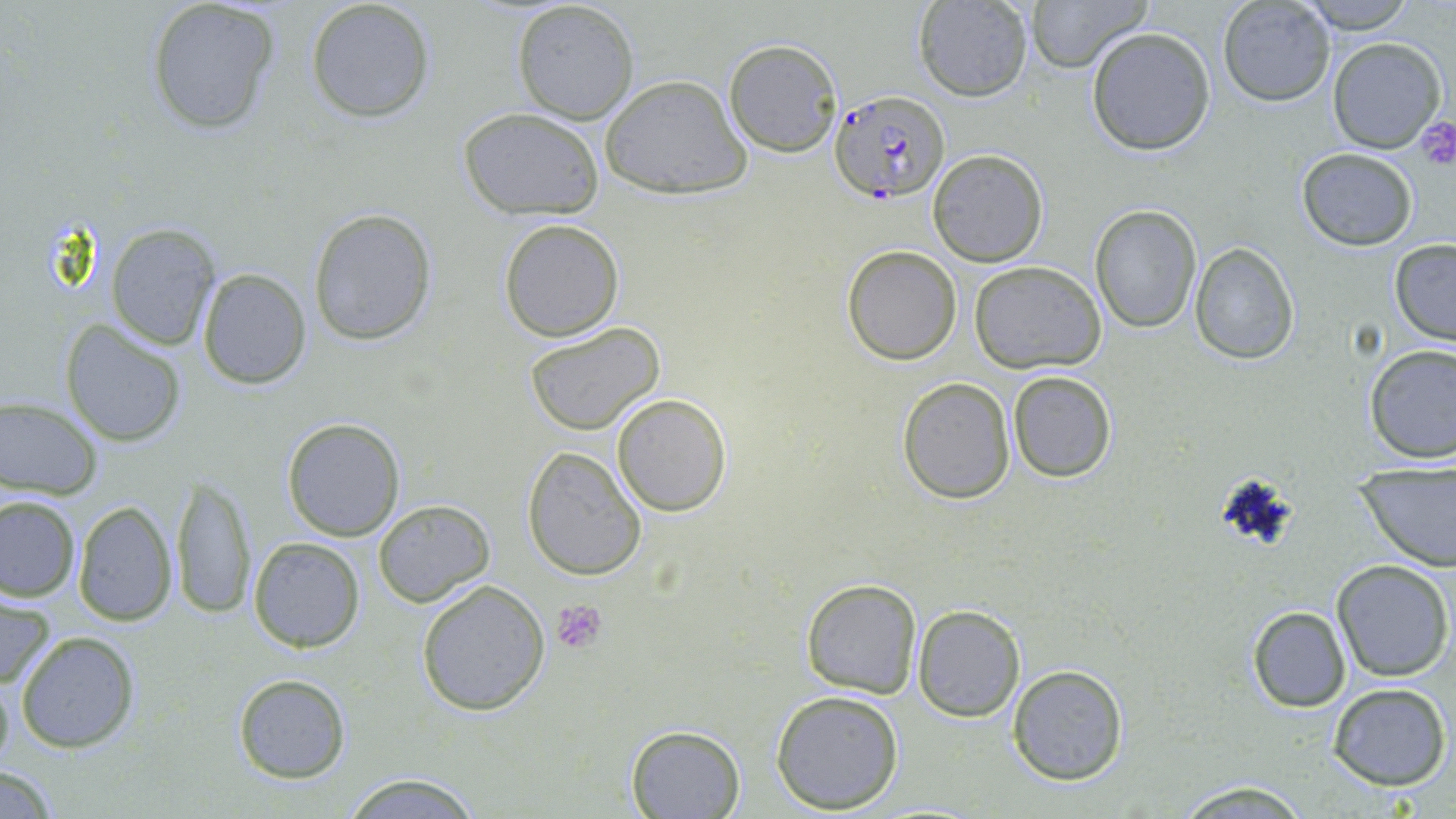

Summary:
  - Coordinate format: approximate bounding boxes as named x1/y1/x2/y2 corners in pixels
  - Uninfected red blood cell locations: (x1=146, y1=0, x2=279, y2=136), (x1=305, y1=0, x2=436, y2=123), (x1=1022, y1=0, x2=1154, y2=73), (x1=1216, y1=0, x2=1336, y2=107), (x1=1297, y1=0, x2=1418, y2=34), (x1=912, y1=1, x2=1034, y2=102), (x1=510, y1=2, x2=640, y2=125), (x1=1086, y1=27, x2=1217, y2=155), (x1=723, y1=37, x2=844, y2=158), (x1=1326, y1=37, x2=1447, y2=154), (x1=600, y1=75, x2=751, y2=199), (x1=458, y1=107, x2=606, y2=218), (x1=1294, y1=146, x2=1419, y2=252), (x1=927, y1=148, x2=1049, y2=267), (x1=1090, y1=204, x2=1202, y2=334), (x1=307, y1=206, x2=438, y2=345), (x1=498, y1=219, x2=624, y2=342), (x1=105, y1=225, x2=221, y2=350), (x1=1388, y1=239, x2=1456, y2=345), (x1=1189, y1=242, x2=1299, y2=365), (x1=842, y1=244, x2=962, y2=366), (x1=970, y1=261, x2=1106, y2=374), (x1=198, y1=268, x2=312, y2=390), (x1=61, y1=322, x2=187, y2=448), (x1=524, y1=322, x2=667, y2=437), (x1=1363, y1=344, x2=1456, y2=464), (x1=1007, y1=369, x2=1117, y2=482), (x1=897, y1=377, x2=1016, y2=503), (x1=612, y1=392, x2=731, y2=517), (x1=0, y1=398, x2=102, y2=499), (x1=281, y1=418, x2=406, y2=541), (x1=522, y1=445, x2=647, y2=580), (x1=1355, y1=462, x2=1456, y2=571), (x1=168, y1=473, x2=259, y2=619), (x1=0, y1=494, x2=80, y2=601), (x1=73, y1=498, x2=177, y2=626), (x1=373, y1=499, x2=495, y2=607), (x1=248, y1=536, x2=366, y2=652), (x1=1332, y1=560, x2=1452, y2=681), (x1=801, y1=578, x2=923, y2=699), (x1=416, y1=580, x2=551, y2=717), (x1=0, y1=589, x2=56, y2=695), (x1=912, y1=604, x2=1025, y2=722), (x1=1246, y1=605, x2=1351, y2=712), (x1=15, y1=631, x2=139, y2=753), (x1=0, y1=665, x2=15, y2=777), (x1=1007, y1=665, x2=1128, y2=784), (x1=233, y1=674, x2=350, y2=784), (x1=1327, y1=682, x2=1451, y2=790), (x1=771, y1=688, x2=904, y2=813), (x1=625, y1=723, x2=746, y2=818), (x1=0, y1=769, x2=64, y2=816), (x1=339, y1=771, x2=483, y2=817), (x1=1170, y1=779, x2=1319, y2=818)
  - Platelet locations: (x1=1412, y1=115, x2=1456, y2=172), (x1=552, y1=599, x2=608, y2=654)
  - Plasmodium falciparum-infected red blood cell locations: (x1=827, y1=89, x2=949, y2=203)
  - Slide-level diagnosis: Plasmodium falciparum
  - Preparation: thin blood film
  - Field of view: single
  - Image size: 1456×819 pixels
  - Modality: optical microscopy
  - Stain: May-Grünwald-Giemsa
  - Magnification: 1000x